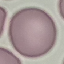

Summary:
  - Malaria status: uninfected
  - Preparation: thin smear
  - Image type: cell patch, automatically extracted from a larger field of view and resized to 64 × 64 pixels
  - Capture: smartphone camera at the microscope eyepiece
  - Stain: Giemsa